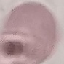

malaria status = uninfected
preparation = thin blood film
image type = automatically extracted cell patch, resized to 64 × 64 pixels
capture = smartphone through the microscope eyepiece
stain = Giemsa